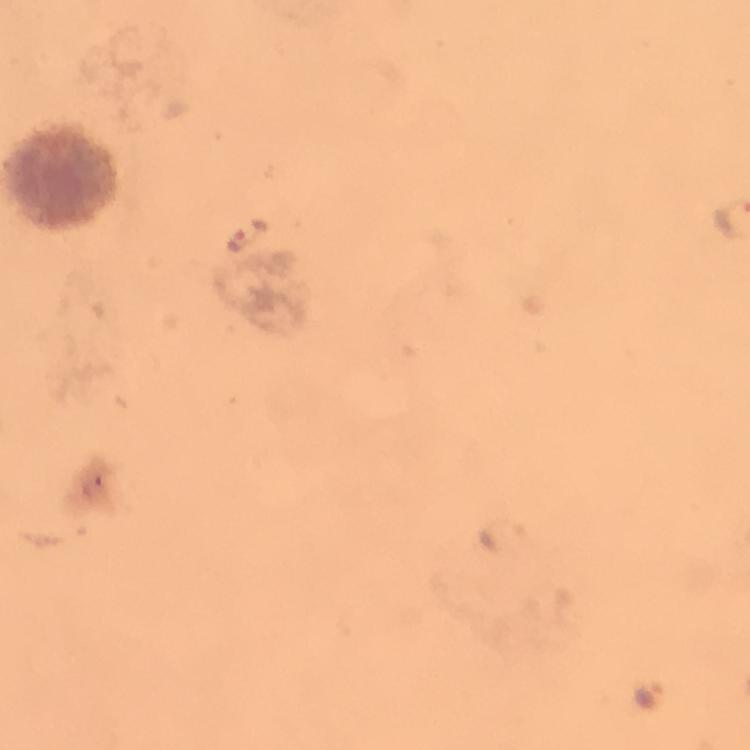

Approximate object centers, in pixels from the top-left corner.
Summary:
  - Plasmodium parasite locations: (x=249, y=236), (x=648, y=697)
  - Capture: smartphone camera through the microscope
  - Image size: 750×750 pixels
  - Immersion oil: applied
  - Context: from a malaria diagnostic workup
  - Cropped from: a single field of view
  - Magnification: 100x
  - Preparation: thick blood film
  - Stain: Giemsa